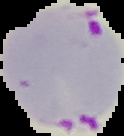 The area outside the segmented cell region is set to black. Malaria status: parasitized. From a thin blood film. Image is 124×136 pixels.